Name the parasite shown.
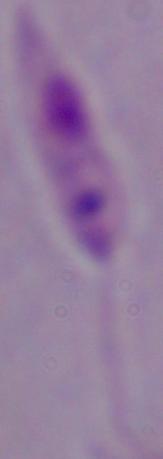
This is Leishmania.

1000x magnification. Micrograph.